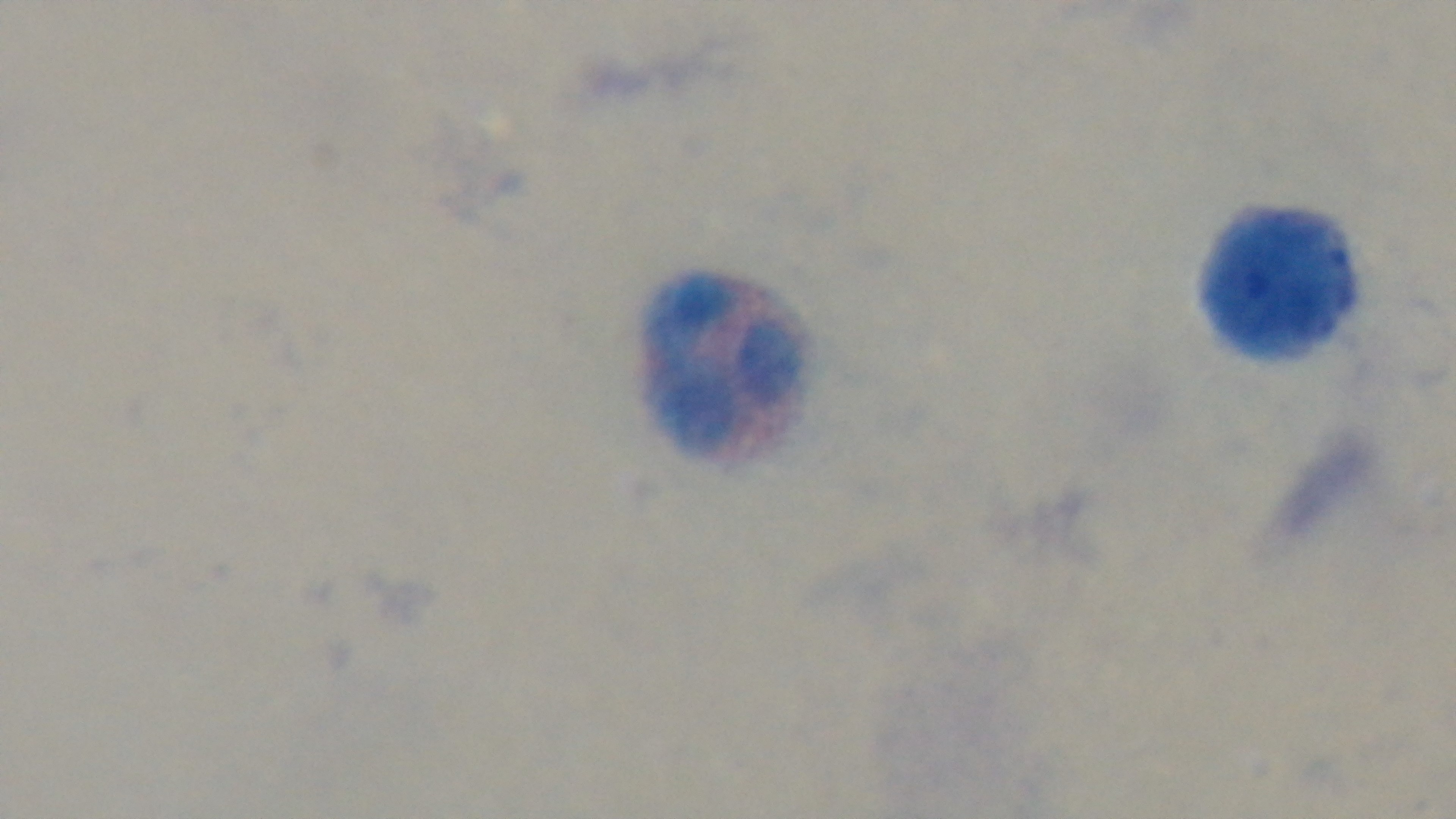

Summary:
  - Capture: mounted 4K digital camera
  - Preparation: thick blood film
  - Field of view: one from the slide
  - Modality: light microscopy
  - Stain: Giemsa
  - Objective: 100x oil immersion
  - Malaria status: negative